Locate every Plasmodium parasite.
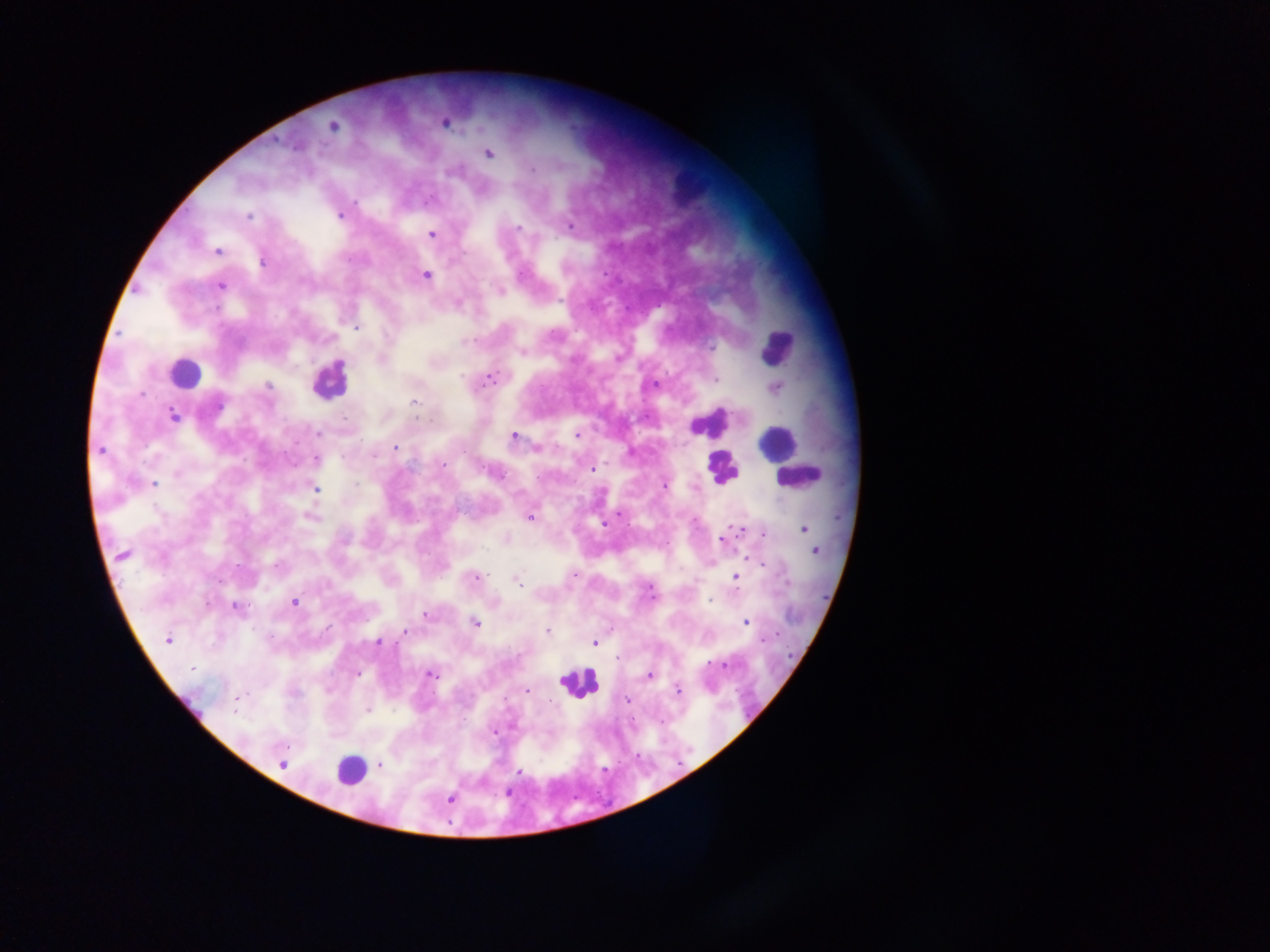
Approximate centers as [x, y] in pixels.
Plasmodium parasites: [445, 123], [332, 126], [488, 154], [532, 169], [430, 199], [355, 202], [248, 216], [339, 216], [570, 225], [519, 228], [432, 235], [217, 252], [263, 262], [425, 275], [220, 285], [498, 290], [558, 299], [216, 309], [356, 328], [468, 341], [710, 346], [521, 352], [489, 379], [716, 379], [268, 385], [654, 385], [775, 389], [141, 394], [414, 402], [218, 405], [174, 416], [344, 418], [417, 418], [318, 434], [576, 434], [513, 437], [395, 448], [536, 448], [100, 451], [316, 458], [443, 464], [591, 469], [502, 476], [153, 484], [355, 484], [665, 485], [316, 490], [618, 514], [310, 517], [529, 517], [603, 525], [741, 529], [804, 529], [764, 534], [722, 539], [814, 550], [123, 554], [750, 559], [711, 563], [763, 564], [276, 565], [476, 578], [736, 579], [517, 582], [710, 601], [294, 602], [236, 608], [424, 615], [475, 622], [746, 622], [404, 631], [547, 632], [167, 640], [764, 640], [378, 642], [595, 643], [616, 658], [711, 663], [724, 666], [192, 669], [357, 673], [430, 675], [650, 675], [677, 690], [526, 691], [236, 699], [628, 700], [550, 701], [368, 711], [493, 732], [282, 764], [380, 765], [518, 772], [508, 794], [450, 799].

Summary:
  - Leukocyte locations: [688, 181], [777, 347], [185, 373], [329, 379], [710, 422], [777, 442], [722, 467], [798, 477], [578, 682], [190, 707], [351, 770]
  - Capture: mobile-phone photograph through a microscope
  - Country: Ghana
  - Field of view: single
  - Image size: 1270×952 pixels
  - Preparation: thick blood film